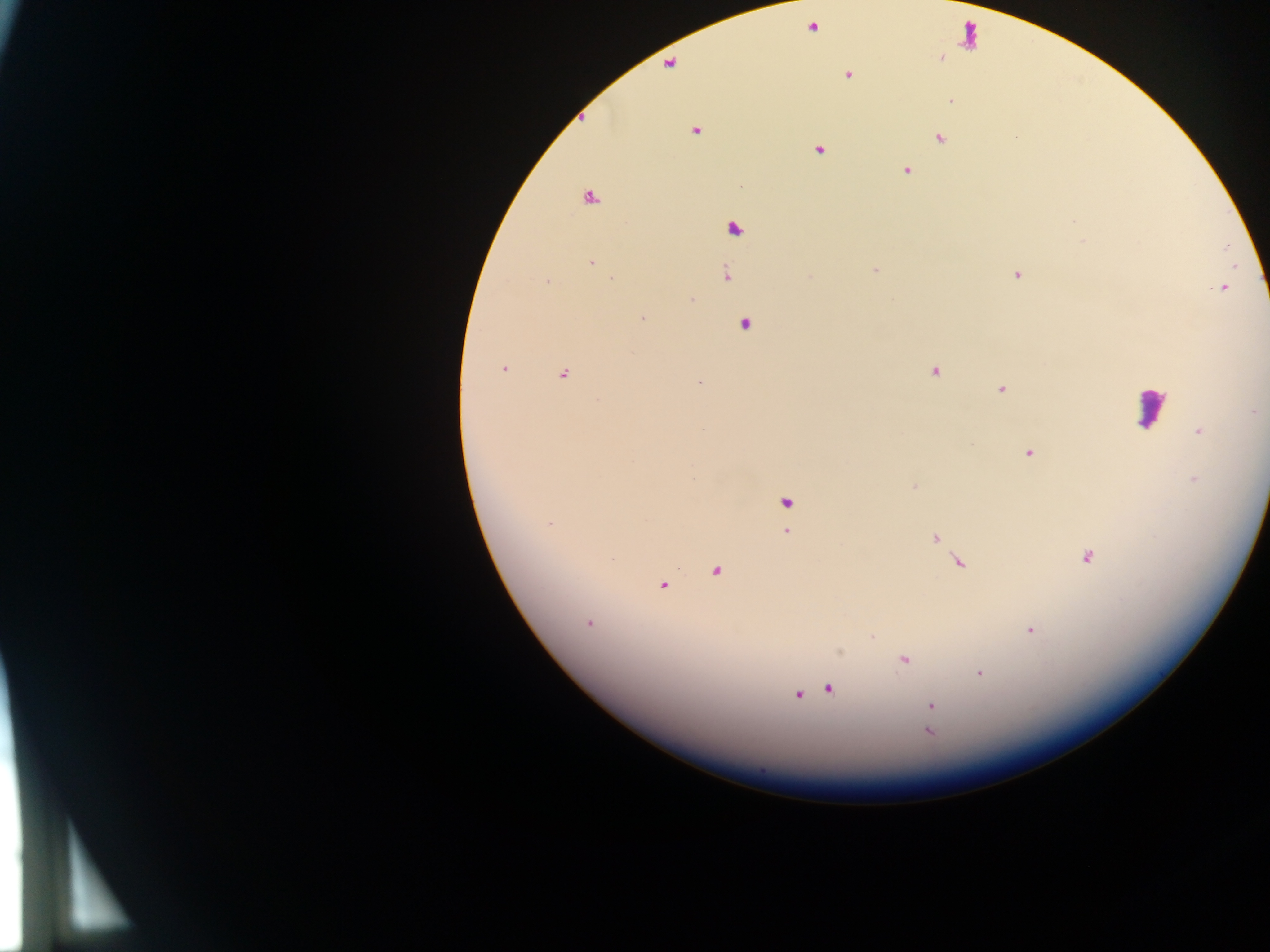

Approximate centers as {x, y} in pixels. Plasmodium parasite locations: {813, 27}, {848, 75}, {952, 101}, {696, 131}, {940, 138}, {819, 149}, {907, 170}, {590, 199}, {1073, 221}, {733, 228}, {591, 262}, {874, 270}, {726, 275}, {1017, 275}, {810, 277}, {612, 279}, {547, 282}, {1222, 288}, {691, 300}, {642, 318}, {744, 324}, {504, 368}, {934, 371}, {563, 374}, {699, 382}, {1001, 389}, {599, 399}, {1255, 412}, {702, 429}, {1199, 431}, {1029, 453}, {693, 478}, {1194, 479}, {914, 486}, {786, 502}, {549, 524}, {787, 532}, {934, 538}, {1086, 557}, {957, 562}, {716, 571}, {663, 585}, {588, 624}, {1030, 631}, {873, 635}, {904, 660}, {980, 673}, {829, 688}, {797, 695}, {931, 705}, {928, 732}. Leukocyte locations: {1151, 407}. Thick blood smear. Collected in Ghana. Photographed through a microscope with a mobile-phone camera. Image is 1270×952 pixels. Single field of view.